Outline each Plasmodium falciparum-infected red blood cell.
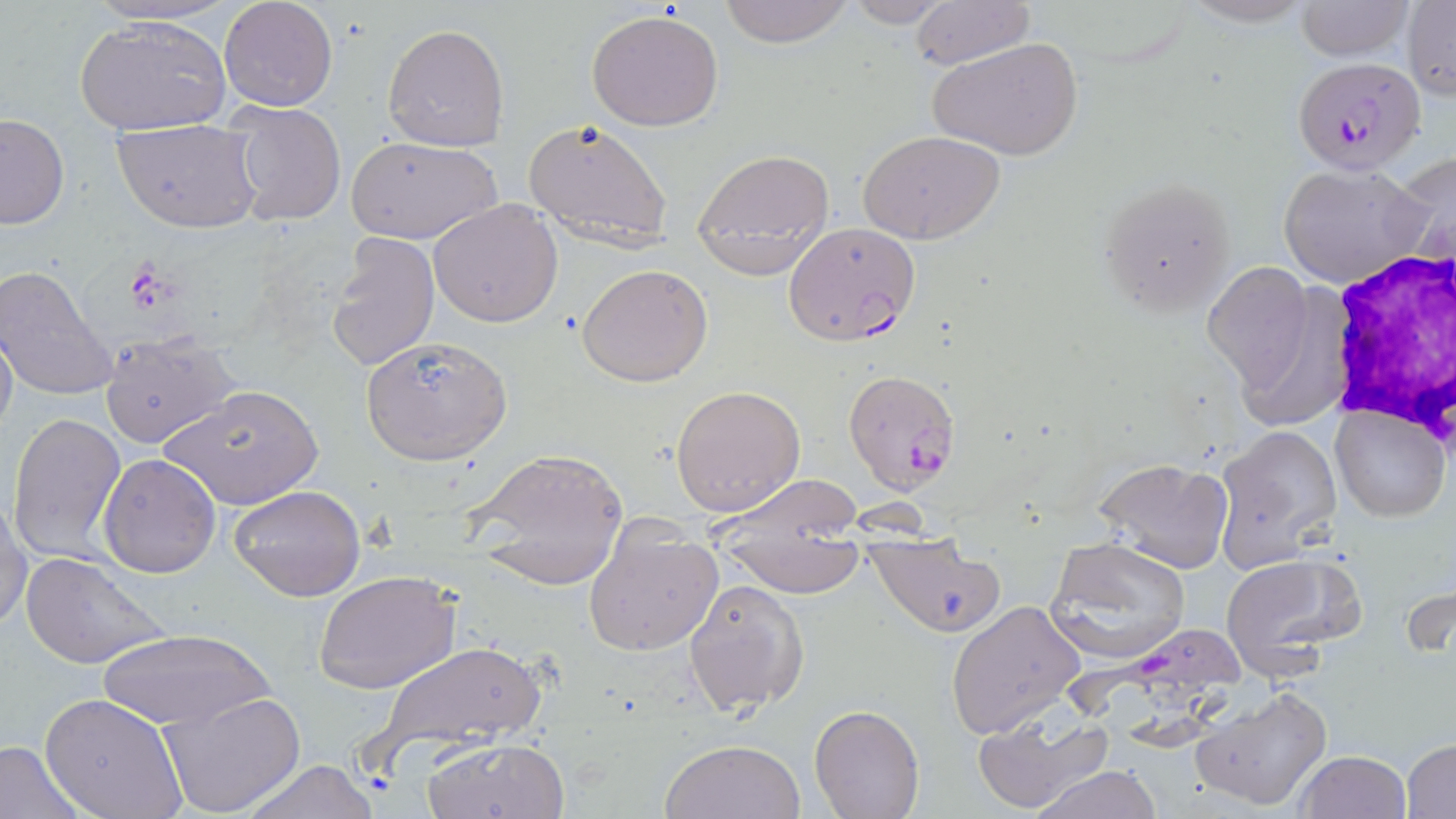

Approximate bounding boxes as named x1/y1/x2/y2 corners in pixels.
Plasmodium falciparum-infected red blood cells: (x1=1293, y1=56, x2=1425, y2=174), (x1=783, y1=222, x2=920, y2=345), (x1=841, y1=369, x2=962, y2=494), (x1=1063, y1=621, x2=1244, y2=763).

Platelet locations: (x1=124, y1=263, x2=175, y2=314). White blood cell locations: (x1=1321, y1=250, x2=1455, y2=451). Uninfected red blood cell locations: (x1=80, y1=0, x2=242, y2=30), (x1=718, y1=0, x2=854, y2=48), (x1=840, y1=0, x2=956, y2=26), (x1=1177, y1=0, x2=1320, y2=27), (x1=218, y1=1, x2=337, y2=112), (x1=910, y1=1, x2=1033, y2=70), (x1=1294, y1=1, x2=1415, y2=62), (x1=1401, y1=1, x2=1456, y2=100), (x1=587, y1=9, x2=726, y2=131), (x1=73, y1=13, x2=232, y2=136), (x1=383, y1=24, x2=509, y2=152), (x1=928, y1=37, x2=1084, y2=160), (x1=227, y1=102, x2=346, y2=226), (x1=0, y1=114, x2=69, y2=231), (x1=113, y1=118, x2=262, y2=233), (x1=521, y1=118, x2=675, y2=251), (x1=860, y1=130, x2=1004, y2=244), (x1=344, y1=135, x2=503, y2=244), (x1=692, y1=148, x2=836, y2=279), (x1=1395, y1=148, x2=1454, y2=276), (x1=1279, y1=161, x2=1431, y2=289), (x1=1097, y1=175, x2=1236, y2=315), (x1=428, y1=198, x2=564, y2=328), (x1=328, y1=232, x2=440, y2=371), (x1=1204, y1=261, x2=1314, y2=390), (x1=577, y1=262, x2=714, y2=386), (x1=0, y1=264, x2=119, y2=403), (x1=0, y1=323, x2=18, y2=445), (x1=358, y1=330, x2=513, y2=465), (x1=100, y1=332, x2=241, y2=450), (x1=158, y1=384, x2=324, y2=512), (x1=671, y1=384, x2=805, y2=517), (x1=1331, y1=403, x2=1449, y2=520), (x1=7, y1=412, x2=126, y2=565), (x1=1215, y1=425, x2=1343, y2=568), (x1=467, y1=450, x2=629, y2=590), (x1=99, y1=455, x2=219, y2=578), (x1=1090, y1=457, x2=1233, y2=574), (x1=711, y1=474, x2=863, y2=542), (x1=228, y1=484, x2=367, y2=602), (x1=1, y1=494, x2=32, y2=634), (x1=583, y1=518, x2=722, y2=660), (x1=1046, y1=535, x2=1191, y2=664), (x1=722, y1=537, x2=868, y2=597), (x1=866, y1=537, x2=1008, y2=637), (x1=20, y1=550, x2=173, y2=670), (x1=1218, y1=553, x2=1364, y2=680), (x1=314, y1=571, x2=460, y2=695), (x1=684, y1=578, x2=809, y2=718), (x1=945, y1=600, x2=1087, y2=741), (x1=96, y1=627, x2=273, y2=730), (x1=369, y1=639, x2=554, y2=762), (x1=1192, y1=684, x2=1334, y2=812), (x1=158, y1=692, x2=306, y2=817), (x1=40, y1=693, x2=189, y2=818), (x1=809, y1=704, x2=925, y2=819), (x1=970, y1=708, x2=1113, y2=812), (x1=423, y1=737, x2=571, y2=819), (x1=660, y1=737, x2=806, y2=819), (x1=1403, y1=738, x2=1456, y2=816), (x1=0, y1=741, x2=86, y2=817), (x1=1294, y1=750, x2=1413, y2=819), (x1=239, y1=759, x2=380, y2=819), (x1=1032, y1=765, x2=1161, y2=819). Slide-level diagnosis: Plasmodium falciparum. May-Grünwald-Giemsa-stained preparation. Light microscopy. One field of a larger specimen. Image is 1456×819 pixels. Thin blood film. Captured at 1000x magnification.